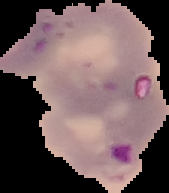 The area outside the segmented cell region is set to black. Image is 169×193 pixels. Result: Plasmodium parasites identified. From a thin blood smear.